Outline each blood parasite and name the species.
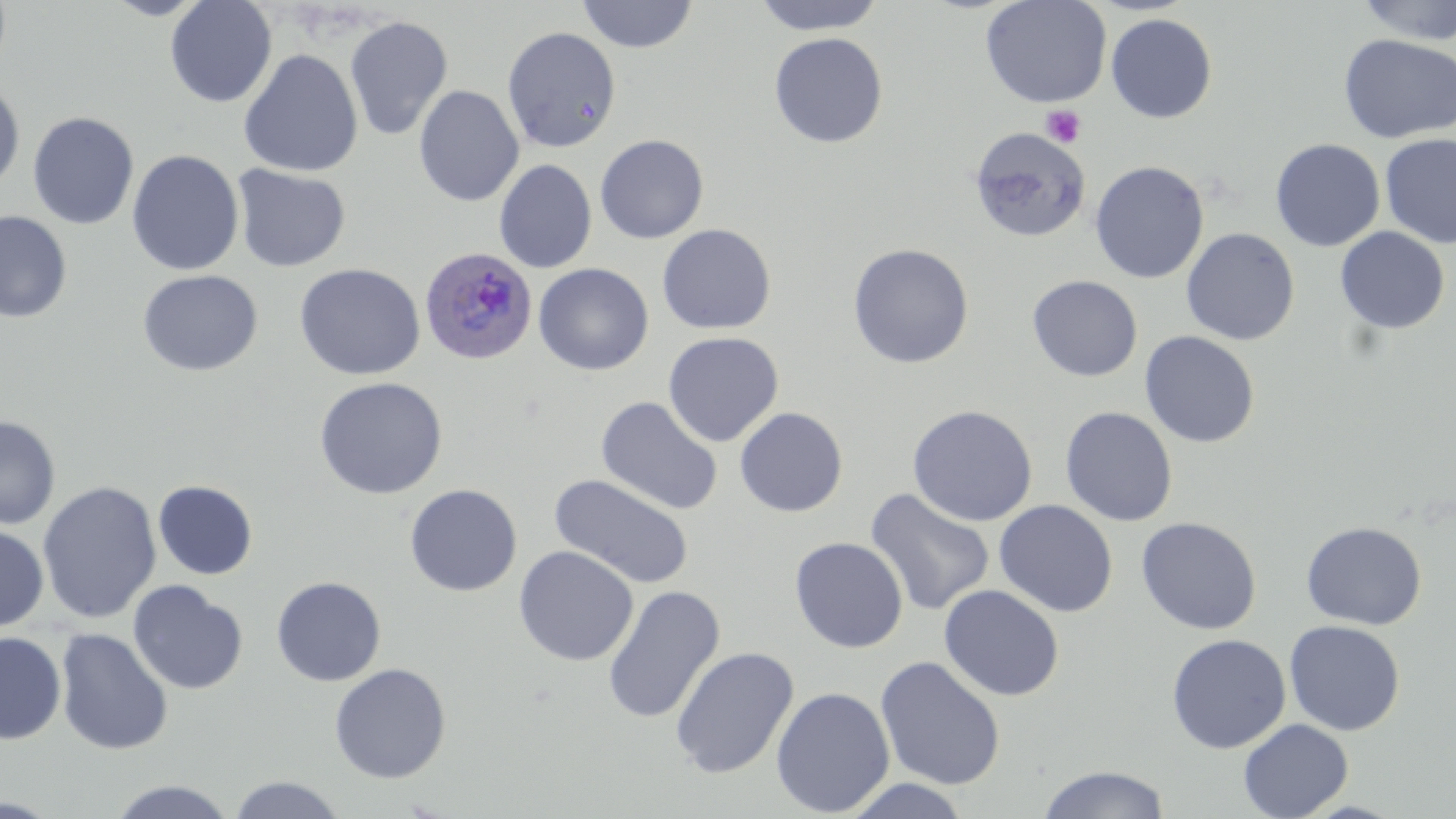

Approximate bounding boxes as (x1,y1)-(x2,y2) corner pairs in pixels.
Plasmodium ovale-infected red blood cells: (419,247)-(539,365).
No Plasmodium falciparum, Plasmodium malariae, Plasmodium vivax, Babesia divergens, or Trypanosoma brucei observed.

Summary:
  - Uninfected red blood cell locations: (102,0)-(212,20), (165,0)-(277,108), (575,0)-(698,53), (751,0)-(887,36), (979,0)-(1112,108), (1354,0)-(1456,45), (1106,13)-(1217,123), (344,15)-(453,141), (502,26)-(621,153), (768,32)-(888,148), (1339,34)-(1456,143), (238,49)-(363,177), (0,79)-(25,195), (413,85)-(524,206), (27,111)-(139,229), (969,127)-(1090,243), (1380,133)-(1456,249), (594,134)-(709,243), (1270,139)-(1385,251), (127,149)-(244,276), (494,159)-(597,273), (1090,160)-(1209,284), (232,164)-(351,273), (0,210)-(72,324), (657,224)-(776,334), (1334,227)-(1450,334), (1181,228)-(1300,346), (847,243)-(974,369), (293,262)-(426,380), (533,263)-(654,376), (137,269)-(263,377), (1027,275)-(1143,381), (1139,330)-(1260,448), (663,332)-(784,447), (313,376)-(448,500), (595,397)-(723,516), (907,405)-(1037,526), (1060,406)-(1178,526), (735,407)-(848,517), (0,415)-(60,529), (550,474)-(694,589), (153,480)-(258,580), (38,481)-(161,624), (405,484)-(522,597), (864,489)-(995,616), (993,499)-(1118,617), (1135,516)-(1262,635), (1301,521)-(1426,630), (0,522)-(49,633), (789,536)-(908,653), (514,546)-(638,666), (271,576)-(387,687), (128,580)-(249,695), (938,584)-(1064,702), (603,585)-(725,725), (1284,620)-(1405,735), (55,628)-(173,755), (0,631)-(66,744), (1167,633)-(1291,754), (670,646)-(799,779), (875,655)-(1006,791), (329,663)-(451,783), (770,686)-(895,817), (1238,718)-(1353,818), (1037,764)-(1171,819), (227,775)-(347,818), (838,778)-(974,818), (105,779)-(239,818)
  - Platelet locations: (1041,105)-(1086,148)
  - Slide-level diagnosis: Plasmodium ovale
  - Image size: 1456×819 pixels
  - Magnification: 1000x
  - Modality: optical microscopy
  - Stain: May-Grünwald-Giemsa
  - Field of view: single
  - Preparation: thin blood film